Locate every uninfected red blood cell.
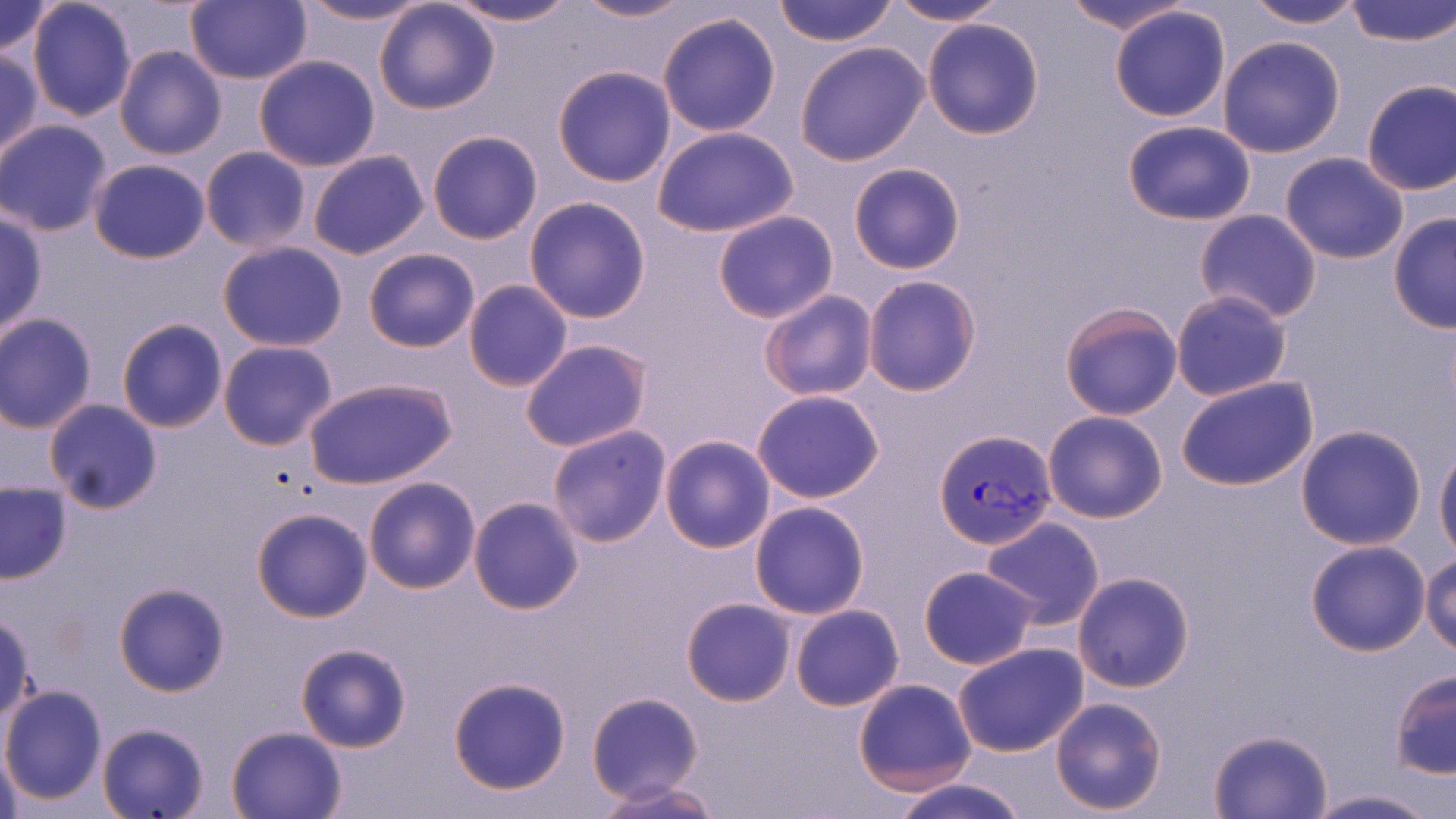

Approximate bounding boxes as named x1/y1/x2/y2 corners in pixels.
Uninfected red blood cells: (x1=0, y1=0, x2=61, y2=59), (x1=26, y1=0, x2=137, y2=120), (x1=184, y1=0, x2=312, y2=85), (x1=294, y1=0, x2=435, y2=26), (x1=570, y1=0, x2=697, y2=23), (x1=773, y1=0, x2=898, y2=46), (x1=887, y1=0, x2=1010, y2=25), (x1=1060, y1=0, x2=1198, y2=34), (x1=1242, y1=0, x2=1367, y2=29), (x1=1346, y1=0, x2=1456, y2=47), (x1=372, y1=1, x2=501, y2=115), (x1=444, y1=1, x2=580, y2=27), (x1=1109, y1=6, x2=1232, y2=122), (x1=656, y1=10, x2=783, y2=137), (x1=921, y1=17, x2=1046, y2=139), (x1=1217, y1=36, x2=1346, y2=157), (x1=795, y1=42, x2=931, y2=167), (x1=114, y1=46, x2=228, y2=162), (x1=0, y1=51, x2=43, y2=161), (x1=254, y1=55, x2=380, y2=172), (x1=552, y1=66, x2=677, y2=187), (x1=1360, y1=79, x2=1456, y2=197), (x1=0, y1=119, x2=113, y2=236), (x1=1121, y1=120, x2=1256, y2=227), (x1=652, y1=125, x2=800, y2=239), (x1=426, y1=129, x2=543, y2=244), (x1=200, y1=147, x2=312, y2=254), (x1=307, y1=150, x2=431, y2=260), (x1=1279, y1=152, x2=1410, y2=265), (x1=89, y1=158, x2=211, y2=263), (x1=848, y1=163, x2=966, y2=275), (x1=524, y1=196, x2=652, y2=323), (x1=1195, y1=209, x2=1323, y2=323), (x1=0, y1=211, x2=47, y2=338), (x1=713, y1=211, x2=838, y2=324), (x1=1388, y1=214, x2=1456, y2=334), (x1=217, y1=241, x2=348, y2=350), (x1=363, y1=248, x2=480, y2=352), (x1=861, y1=275, x2=983, y2=396), (x1=463, y1=279, x2=574, y2=392), (x1=757, y1=290, x2=878, y2=402), (x1=1170, y1=290, x2=1293, y2=402), (x1=1058, y1=300, x2=1185, y2=421), (x1=0, y1=313, x2=98, y2=433), (x1=117, y1=318, x2=229, y2=434), (x1=520, y1=339, x2=653, y2=452), (x1=217, y1=340, x2=340, y2=451), (x1=305, y1=377, x2=458, y2=490), (x1=1175, y1=377, x2=1319, y2=493), (x1=751, y1=389, x2=885, y2=503), (x1=43, y1=401, x2=162, y2=515), (x1=1043, y1=410, x2=1168, y2=524), (x1=1295, y1=424, x2=1426, y2=550), (x1=547, y1=425, x2=673, y2=548), (x1=660, y1=435, x2=775, y2=554), (x1=1435, y1=442, x2=1456, y2=561), (x1=363, y1=476, x2=480, y2=595), (x1=0, y1=481, x2=73, y2=584), (x1=468, y1=496, x2=584, y2=614), (x1=750, y1=501, x2=870, y2=619), (x1=251, y1=507, x2=375, y2=623), (x1=982, y1=517, x2=1105, y2=629), (x1=1304, y1=540, x2=1431, y2=656), (x1=1420, y1=552, x2=1456, y2=656), (x1=919, y1=566, x2=1038, y2=669), (x1=1073, y1=571, x2=1195, y2=693), (x1=112, y1=581, x2=230, y2=697), (x1=682, y1=598, x2=795, y2=705), (x1=790, y1=604, x2=904, y2=711), (x1=0, y1=614, x2=36, y2=723), (x1=952, y1=641, x2=1089, y2=758), (x1=295, y1=642, x2=411, y2=753), (x1=1389, y1=670, x2=1455, y2=780), (x1=447, y1=677, x2=573, y2=796), (x1=852, y1=678, x2=978, y2=794), (x1=0, y1=685, x2=107, y2=805), (x1=587, y1=692, x2=704, y2=805), (x1=1049, y1=696, x2=1168, y2=816), (x1=95, y1=721, x2=212, y2=819), (x1=226, y1=724, x2=348, y2=818), (x1=1206, y1=728, x2=1335, y2=818), (x1=1, y1=747, x2=27, y2=819), (x1=888, y1=777, x2=1030, y2=819), (x1=591, y1=779, x2=724, y2=818), (x1=1300, y1=788, x2=1445, y2=819).

Plasmodium vivax-infected red blood cell locations: (x1=934, y1=429, x2=1056, y2=551). Slide-level diagnosis: Plasmodium vivax. One field of a larger specimen. Optical microscopy. Thin blood film. May-Grünwald-Giemsa-stained preparation. Image is 1456×819 pixels. 1000x magnification.